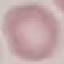

result = negative for malaria parasites
capture = smartphone camera at the microscope eyepiece
image type = automatically extracted cell patch, resized to 64 × 64 pixels
preparation = thin blood film
stain = Giemsa